Identify the blood parasite species.
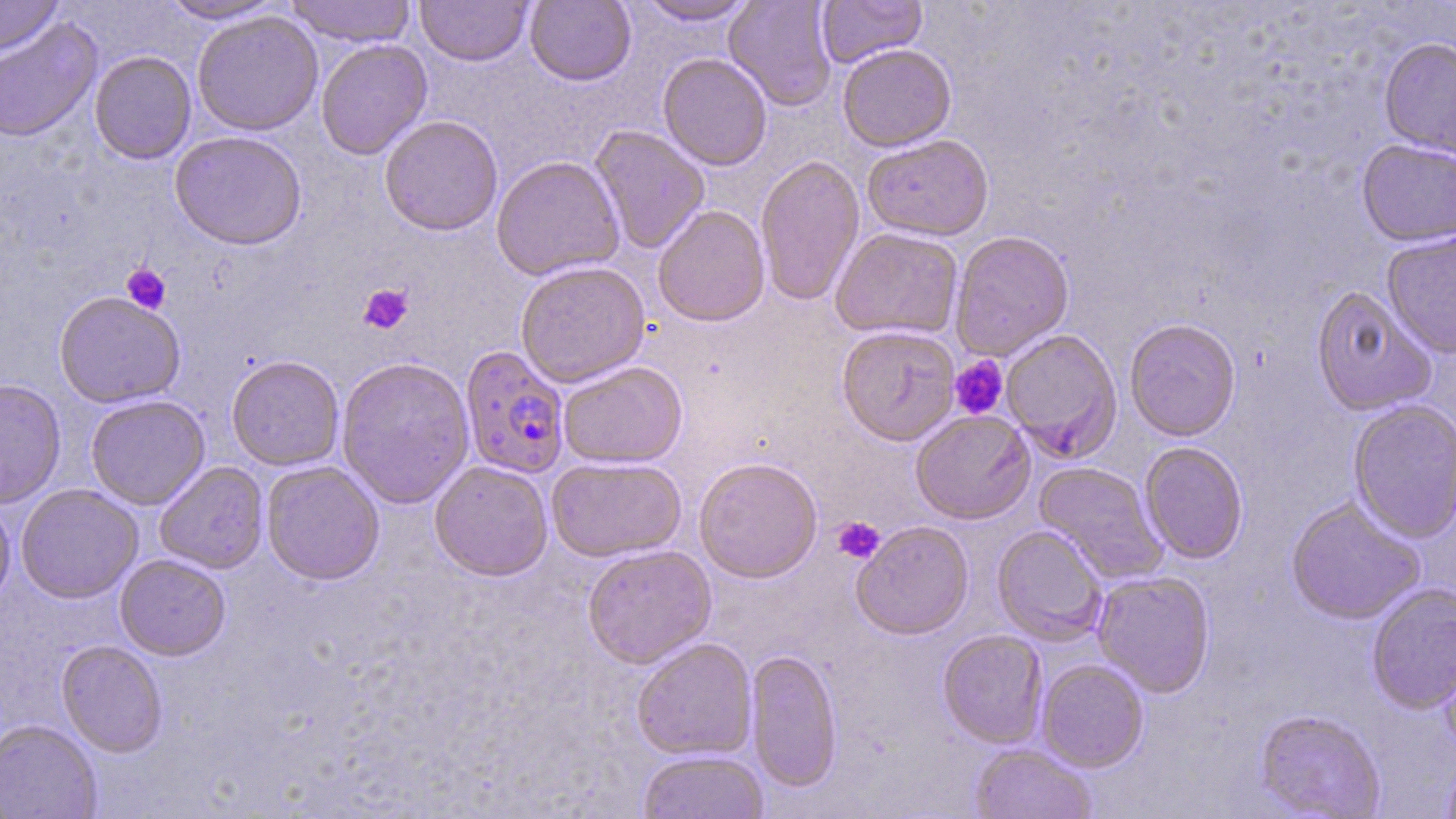

Plasmodium falciparum.

Summary:
  - Coordinate format: approximate bounding boxes as [x1, y1, x2, y2] in pixels
  - Plasmodium falciparum-infected red blood cell locations: [459, 346, 570, 479]
  - Uninfected red blood cell locations: [0, 0, 64, 56], [157, 0, 288, 24], [284, 0, 417, 47], [415, 0, 533, 66], [524, 0, 636, 86], [634, 0, 760, 25], [724, 0, 837, 111], [817, 0, 927, 68], [191, 11, 324, 136], [0, 18, 102, 143], [315, 39, 432, 160], [1379, 39, 1456, 159], [838, 44, 956, 151], [89, 51, 197, 164], [657, 53, 773, 170], [379, 115, 503, 236], [589, 125, 710, 254], [170, 131, 307, 250], [862, 134, 994, 241], [1357, 141, 1456, 249], [755, 155, 864, 306], [491, 156, 625, 280], [653, 205, 770, 327], [830, 227, 963, 340], [1381, 230, 1456, 358], [950, 231, 1074, 360], [515, 261, 650, 387], [1310, 286, 1436, 416], [54, 291, 185, 408], [1124, 319, 1241, 442], [836, 326, 960, 446], [1001, 329, 1122, 463], [226, 355, 344, 471], [335, 356, 475, 509], [558, 360, 688, 468], [0, 378, 66, 508], [86, 394, 209, 510], [1347, 400, 1456, 543], [910, 410, 1035, 524], [1139, 442, 1248, 564], [546, 456, 686, 562], [694, 457, 822, 582], [261, 460, 385, 585], [429, 460, 553, 580], [154, 461, 269, 574], [1033, 461, 1168, 584], [15, 484, 143, 603], [0, 497, 15, 612], [1286, 497, 1425, 625], [851, 521, 974, 640], [992, 525, 1107, 645], [582, 545, 716, 668], [115, 554, 231, 660], [1092, 571, 1215, 698], [1366, 583, 1456, 715], [937, 630, 1048, 748], [1437, 634, 1456, 757], [632, 638, 757, 761], [56, 640, 167, 758], [745, 649, 842, 793], [1036, 659, 1148, 772], [1254, 709, 1385, 818], [0, 720, 102, 819], [970, 743, 1097, 819], [638, 750, 769, 819], [1441, 757, 1456, 819]
  - Platelet locations: [121, 263, 171, 314], [358, 283, 413, 335], [949, 356, 1009, 420], [832, 516, 885, 563]
  - Magnification: 1000x
  - Modality: optical microscopy
  - Image size: 1456×819 pixels
  - Stain: May-Grünwald-Giemsa
  - Field of view: one of a larger specimen
  - Preparation: thin blood film